Report the malaria status of this cell.
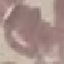

Uninfected.

Thin blood smear. Photographed with a smartphone camera at the microscope eyepiece. Giemsa-stained preparation. Automatically extracted cell patch, resized to 64 × 64 pixels.